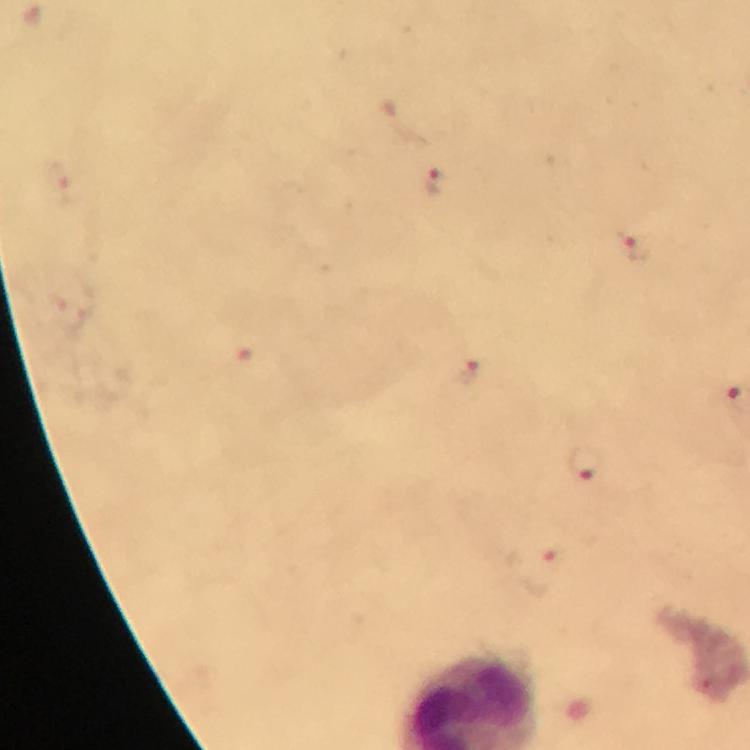
cropped from = a single field of view
capture = smartphone mounted on the microscope
magnification = 100x
immersion oil = applied
stain = Giemsa
image size = 750×750 pixels
Plasmodium parasite locations = approximate centers as (x, y) in pixels: (32, 16), (434, 182), (637, 249), (469, 371), (585, 463), (548, 558)
preparation = thick smear
context = from a diagnostic examination for malaria